Mark where platelets are.
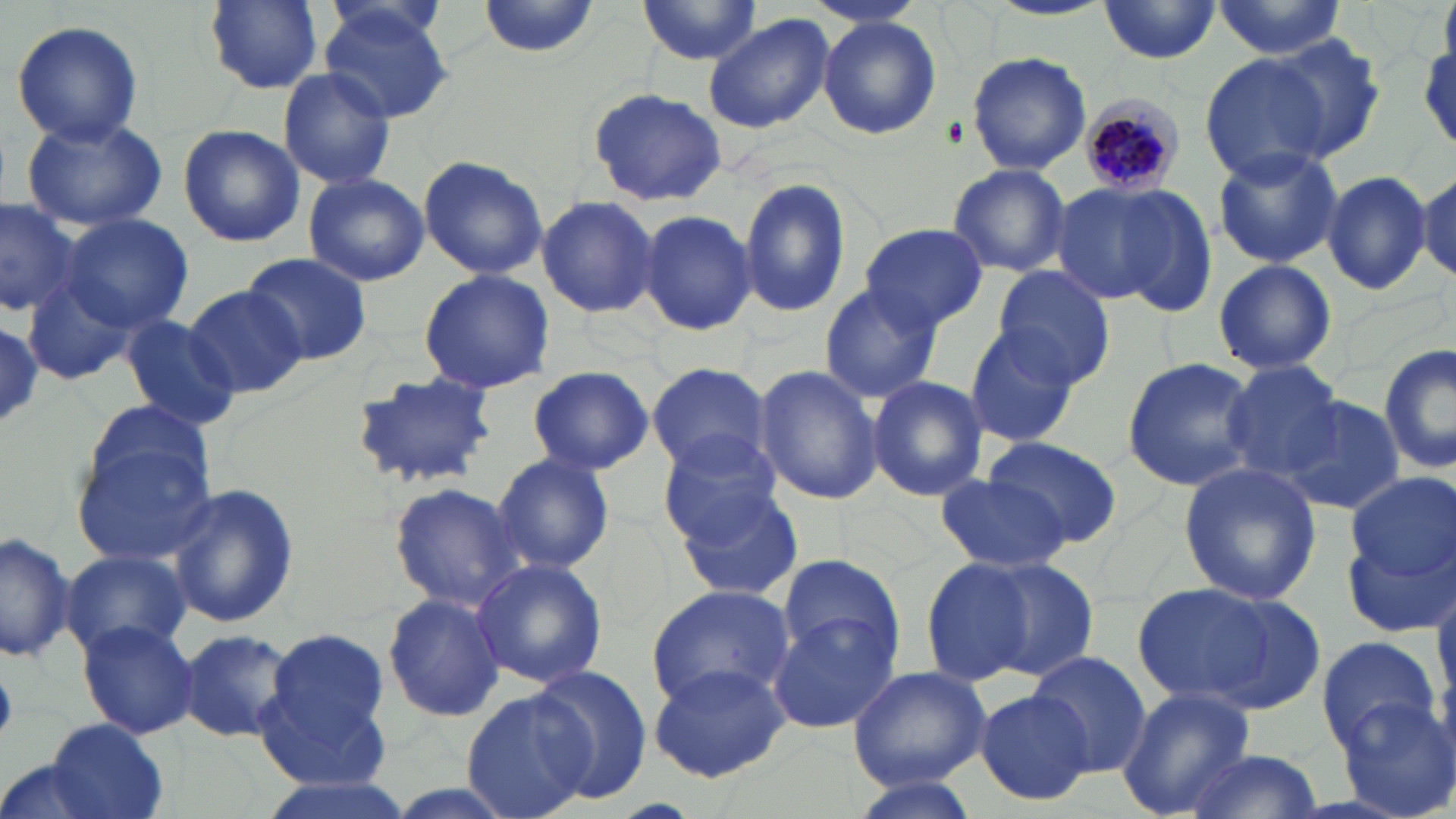

Approximate bounding boxes as (x1,y1)-(x2,y2) corner pairs in pixels.
Platelets: (0,671)-(17,743).

Uninfected red blood cell locations: (199,0)-(326,95), (478,0)-(601,58), (640,0)-(766,68), (985,1)-(1114,21), (1098,1)-(1224,66), (318,2)-(453,122), (1210,3)-(1350,57), (703,13)-(835,132), (817,17)-(942,139), (10,19)-(145,145), (1267,35)-(1385,158), (966,51)-(1092,174), (1199,53)-(1334,182), (276,66)-(399,190), (588,86)-(726,206), (21,114)-(169,233), (177,124)-(305,247), (1210,143)-(1343,269), (417,154)-(547,280), (947,163)-(1071,277), (1320,169)-(1432,297), (1416,171)-(1455,285), (301,173)-(430,285), (737,177)-(850,320), (1058,178)-(1205,309), (535,195)-(662,319), (0,197)-(84,319), (635,207)-(757,337), (58,212)-(194,336), (860,223)-(987,332), (242,253)-(372,364), (1212,257)-(1337,375), (992,267)-(1118,388), (416,269)-(555,393), (24,274)-(138,385), (819,283)-(944,403), (184,285)-(304,400), (119,313)-(241,430), (963,320)-(1086,446), (0,324)-(45,426), (1378,343)-(1456,475), (1121,356)-(1259,492), (1224,360)-(1349,483), (647,363)-(773,476), (753,365)-(880,506), (525,366)-(654,475), (349,371)-(502,489), (867,376)-(988,502), (1279,395)-(1406,514), (85,399)-(215,504), (661,434)-(786,547), (982,435)-(1123,548), (71,436)-(217,570), (492,453)-(615,575), (1176,462)-(1321,605), (1345,473)-(1454,582), (935,475)-(1070,573), (169,483)-(298,629), (388,483)-(524,612), (671,486)-(804,603), (1342,527)-(1454,639), (0,529)-(78,663), (61,550)-(191,660), (777,552)-(905,663), (918,556)-(1039,690), (977,556)-(1100,680), (470,558)-(608,689), (1432,571)-(1456,708), (1134,580)-(1325,715), (646,583)-(794,707), (382,590)-(506,722), (768,613)-(899,733), (77,618)-(200,738), (259,626)-(395,778), (176,628)-(297,743), (1315,634)-(1441,751), (1026,653)-(1153,774), (648,660)-(793,784), (847,662)-(992,791), (529,666)-(653,803), (463,686)-(594,819), (1117,687)-(1256,817), (974,688)-(1095,805), (1335,700)-(1456,818), (41,719)-(168,819), (1184,749)-(1322,818), (0,755)-(123,819), (250,770)-(417,819), (845,775)-(983,819). Plasmodium malariae-infected red blood cell locations: (1078,96)-(1186,198). Slide-level diagnosis: Plasmodium malariae. One field of a larger specimen. Optical microscopy. May-Grünwald-Giemsa-stained preparation. Image is 1456×819 pixels. Captured at 1000x magnification. Thin blood film.